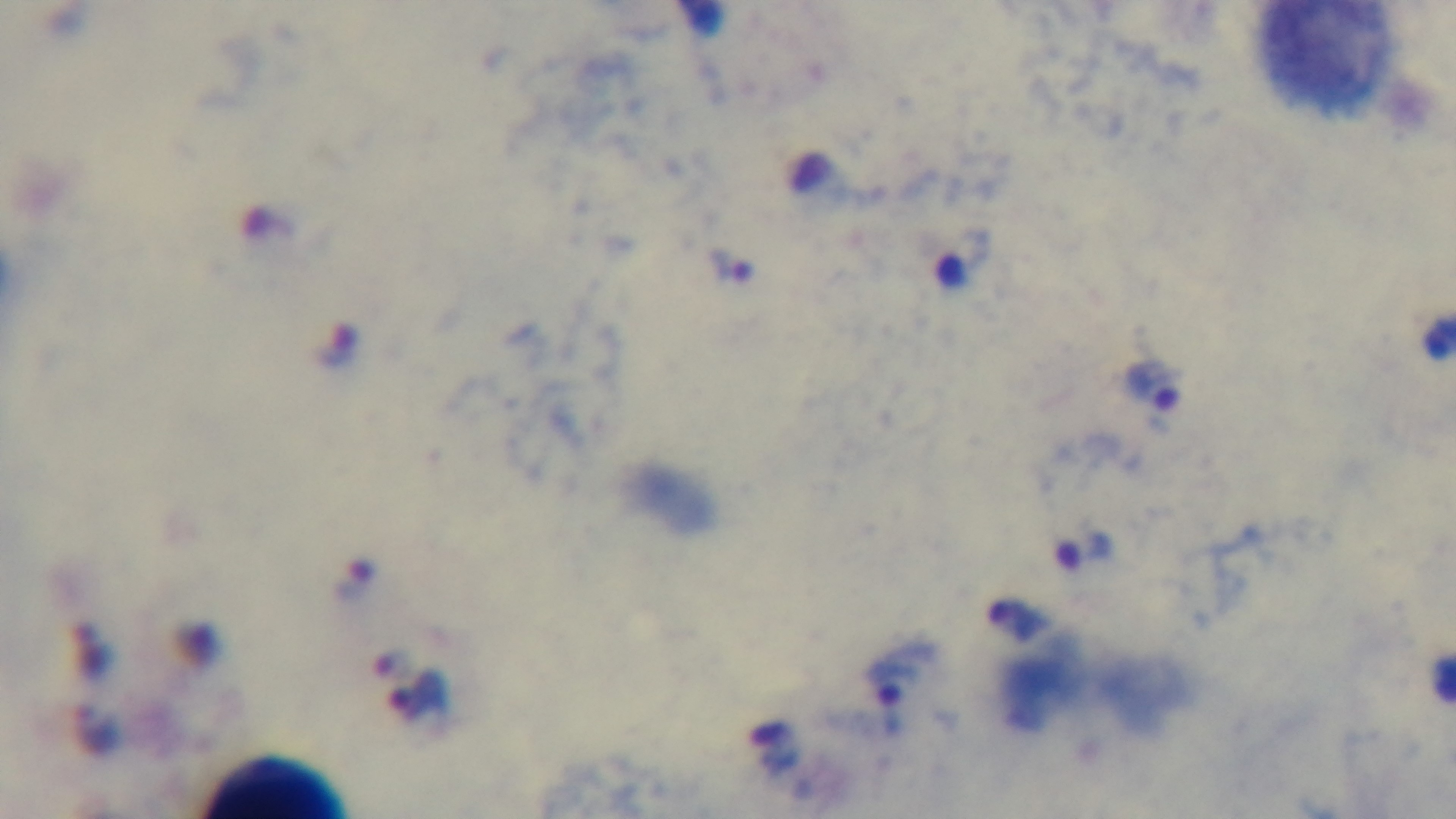

Summary:
  - Objective: 100x oil immersion
  - Field of view: single
  - Stain: Giemsa
  - Capture: mounted 4K digital camera
  - Preparation: thick smear
  - Modality: light microscopy
  - Malaria status: infected